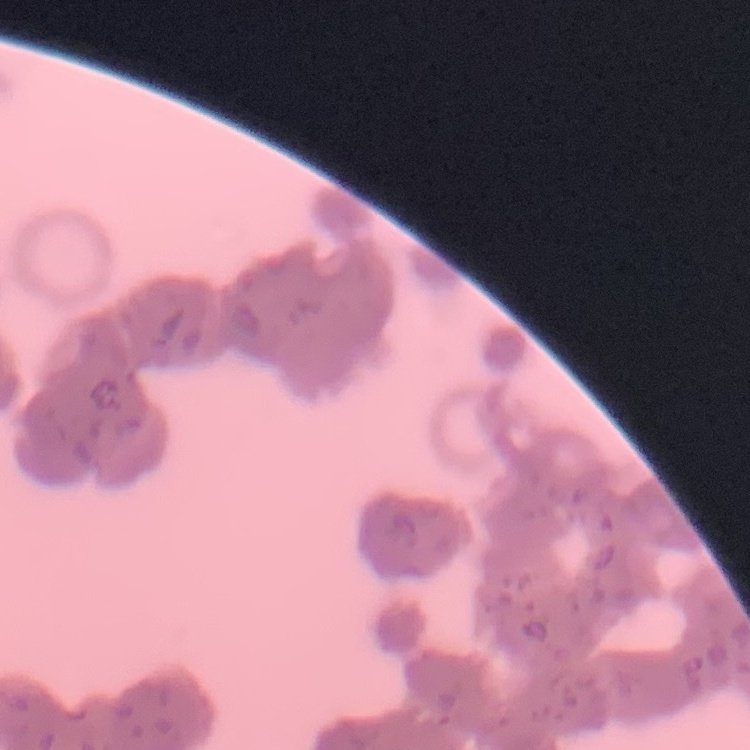
erythrocyte morphology = rouleaux formation
image type = one tile cut from a larger photomicrograph
preparation = thin peripheral smear
stain = Field's or Giemsa